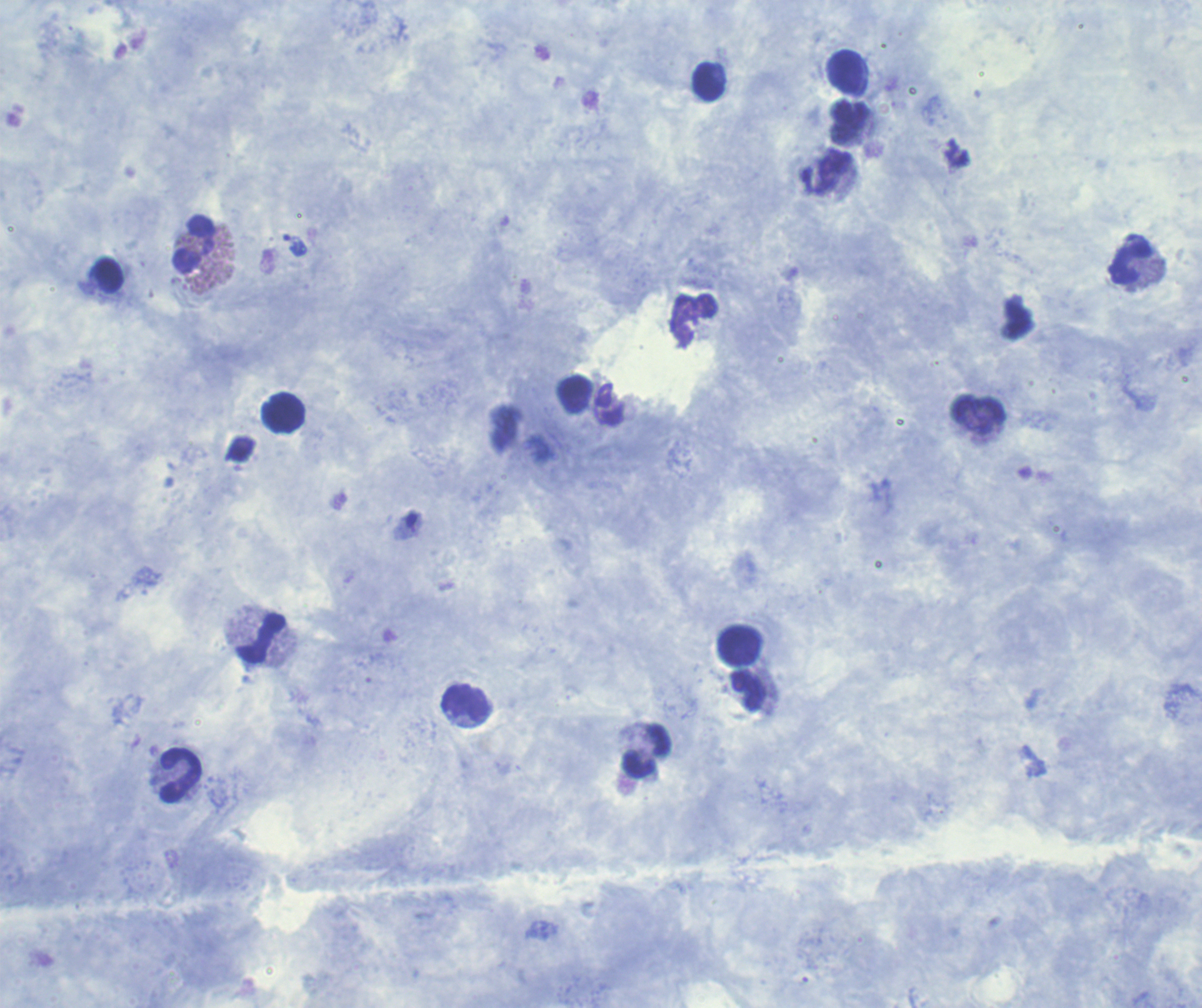
Approximate centers as [x, y] in pixels.
Summary:
  - Trophozoite locations: [294, 245]
  - Leukocyte locations: [844, 72], [708, 82], [848, 121], [194, 245], [1130, 263], [108, 276], [574, 394], [282, 413], [978, 415], [261, 639], [739, 646], [747, 690], [464, 702], [647, 751], [180, 775]
  - Stain: Romanowsky
  - Background quality: good
  - Coloration quality: good
  - Preparation: thick blood film
  - Result: malaria parasites detected
  - Field of view: one from this slide
  - Context: previously used in an actual diagnosis
  - Image size: 1202×1008 pixels
  - Magnification: 100x